Identify the parasite.
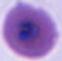
Plasmodium.

Summary:
  - Magnification: 400x or 1000x
  - Modality: photomicrograph